Point out every Plasmodium parasite.
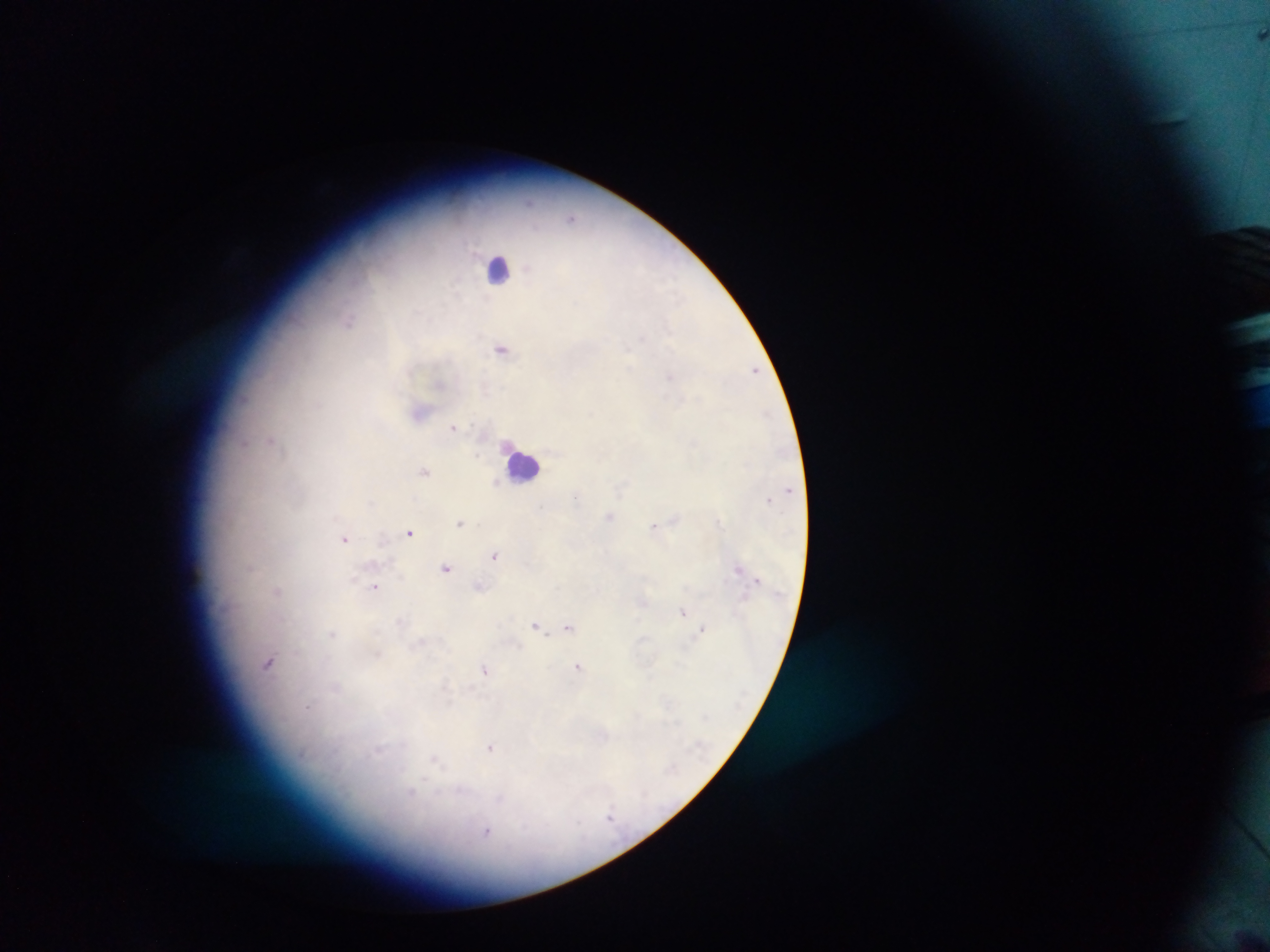

Approximate centers as (x, y) in pixels.
Plasmodium parasites: (1260, 35), (571, 218), (349, 321), (641, 337), (501, 349), (628, 350), (754, 370), (670, 376), (453, 427), (271, 441), (245, 444), (477, 455), (425, 472), (497, 481), (770, 499), (372, 503), (540, 506), (609, 516), (674, 519), (460, 522), (653, 527), (410, 533), (344, 538), (494, 555), (251, 567), (446, 568), (738, 568), (757, 580), (479, 586), (374, 587), (278, 591), (683, 612), (536, 625), (568, 627), (702, 628), (332, 634), (269, 663), (578, 667), (485, 669), (308, 707), (490, 747), (435, 759), (411, 793), (610, 815), (487, 832).

Summary:
  - Leukocyte locations: (498, 268), (524, 465)
  - Field of view: single
  - Country: Ghana
  - Preparation: thick blood film
  - Capture: mobile-phone photograph through a microscope
  - Image size: 1270×952 pixels